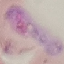

Result: malaria parasites identified. Acquired by smartphone through the microscope eyepiece. Automatically extracted cell patch, resized to 64 × 64 pixels. Thin blood film. Giemsa-stained preparation.